Name the parasite shown.
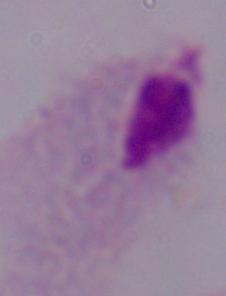

A trichomonad.

Summary:
  - Modality: photomicrograph
  - Magnification: 1000x